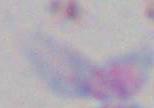
magnification: 1000x
identification: Toxoplasma gondii
modality: photomicrograph